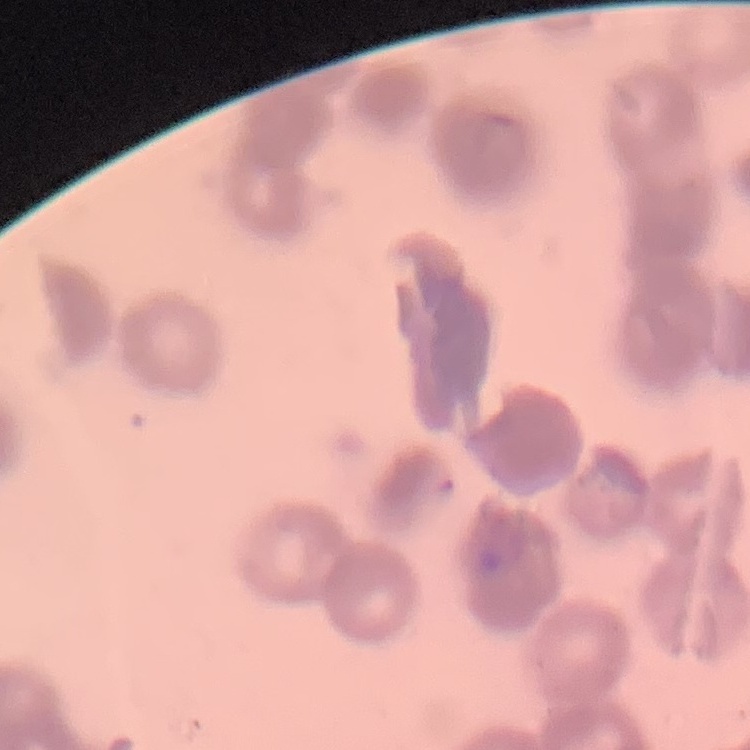 The erythrocytes show rouleaux formation. Stained with either Field's or Giemsa. Thin blood film. Square crop of a larger photomicrograph.